Identify the parasite.
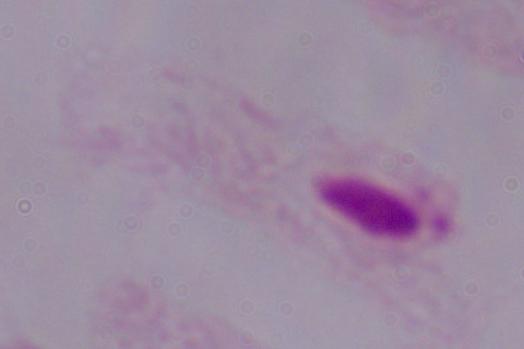

This is a trichomonad.

Micrograph. 1000x magnification.